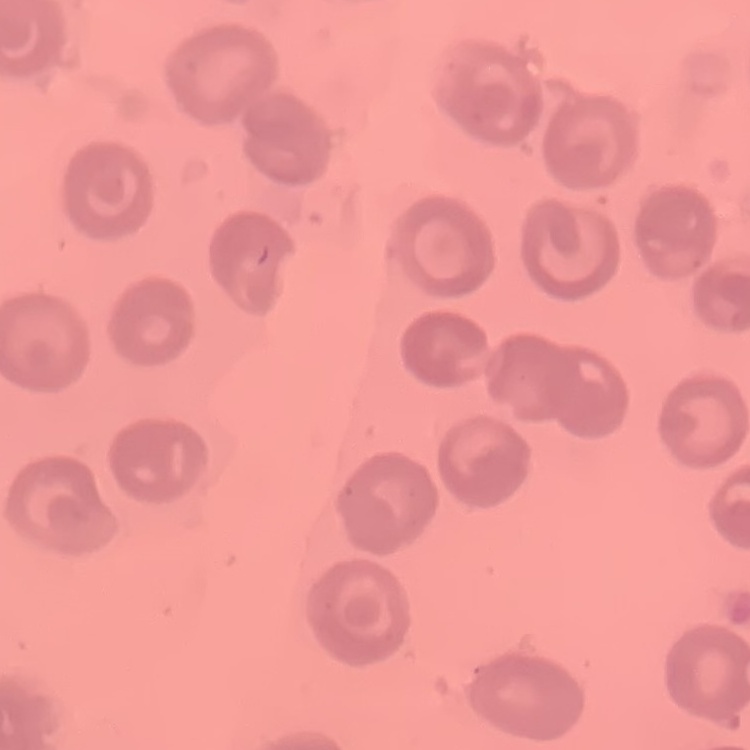

Summary:
  - Erythrocyte morphology: no rouleaux formation
  - Image type: square crop of a larger photomicrograph
  - Stain: Field's or Giemsa
  - Preparation: thin blood film